Assess for malaria.
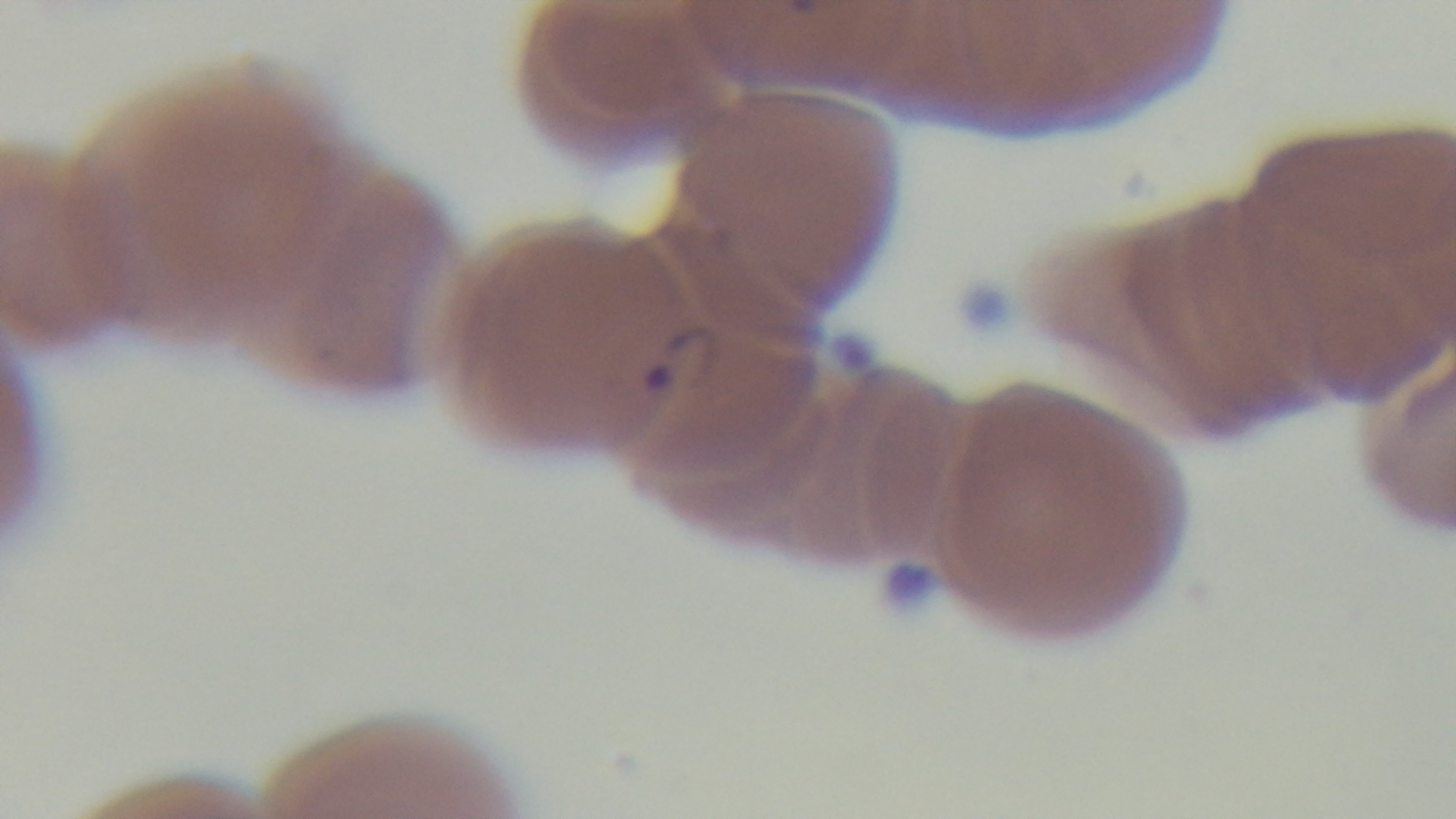
Positive.

100x oil-immersion objective. One field from the slide. Giemsa stain. Preparation: thin. Photomicrograph. Captured with a mounted 4K digital camera.